Name the parasite shown.
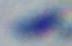
This is Toxoplasma gondii.

Summary:
  - Modality: micrograph
  - Magnification: 1000x